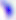

{
  "modality": "micrograph",
  "magnification": "400x",
  "identification": "Toxoplasma gondii"
}